Locate every malaria parasite.
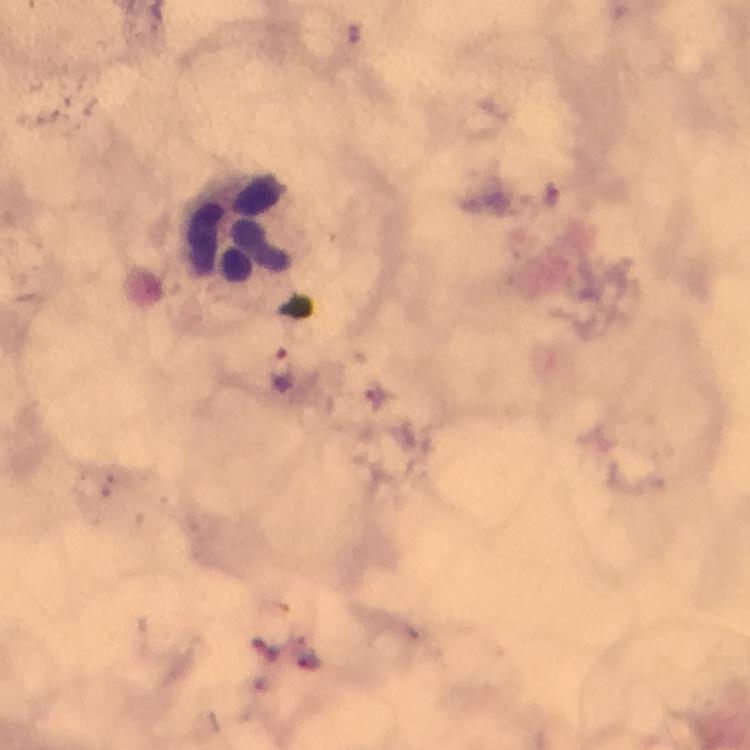
Approximate centers as (x, y) in pixels.
Malaria parasites: (552, 196), (280, 371), (374, 391), (308, 661).

Leukocyte locations: (234, 226). From a diagnostic examination for malaria. Giemsa stain. At 100x magnification. Image is 750×750 pixels. A crop from one field of view. Immersion oil was used. Photographed with a smartphone mounted on the microscope. Thick blood film.